Classify this cell by malaria status.
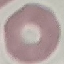
It is uninfected.

Summary:
  - Preparation: thin blood film
  - Stain: Giemsa
  - Image type: automatically extracted cell patch, resized to 64 × 64 pixels
  - Capture: smartphone through the microscope eyepiece